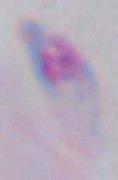
Summary:
  - Identification: Toxoplasma gondii
  - Modality: photomicrograph
  - Magnification: 1000x